Point out each malaria parasite and classify it by life-cycle stage.
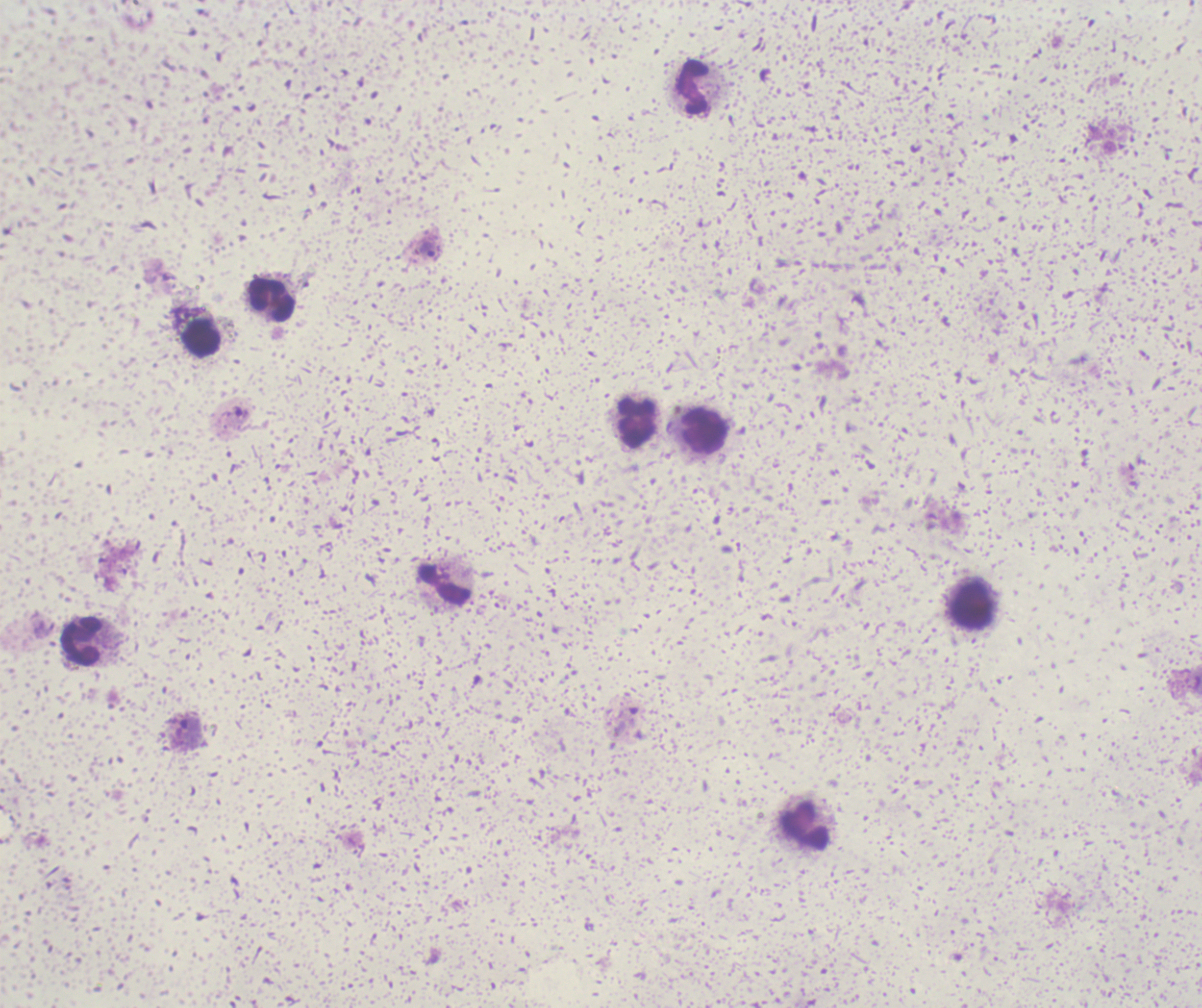
Approximate object centers, in pixels from the top-left corner.
Trophozoites: (x=429, y=250), (x=189, y=729).
No schizont or gametocyte forms observed.

Approximate object centers, in pixels from the top-left corner. Leukocyte locations: (x=693, y=87), (x=272, y=300), (x=202, y=337), (x=639, y=424), (x=704, y=430), (x=446, y=584), (x=973, y=605), (x=81, y=641), (x=805, y=826). Background quality: poor. Image is 1202×1008 pixels. Thick blood film. Captured at 100x magnification. Romanowsky stain. Single field of view. Previously used in an actual diagnosis.